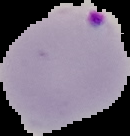
image type = cell region segmented out of the field of view; surrounding area masked to black
preparation = thin blood smear
malaria status = parasitized
image size = 130×136 pixels